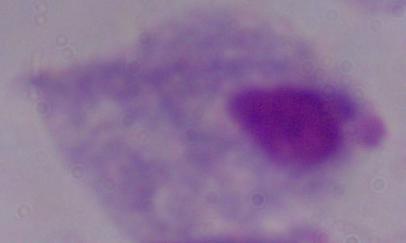 Micrograph. A trichomonad is shown. Captured at 1000x magnification.